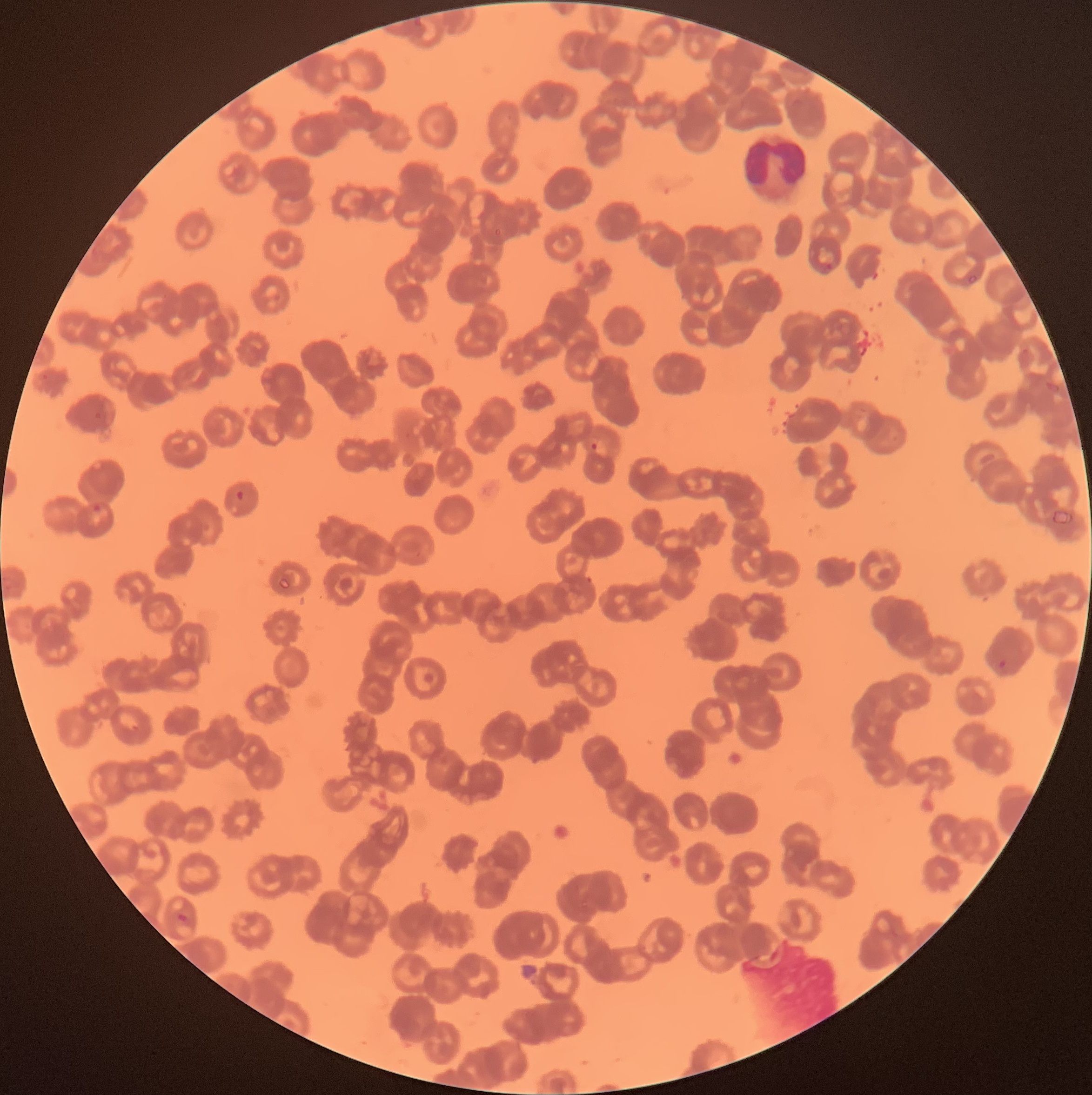

coordinate format = approximate bounding boxes as named x1/y1/x2/y2 corners in pixels
white blood cell locations = (x1=741, y1=134, x2=809, y2=205)
Plasmodium parasite locations = (x1=820, y1=261, x2=834, y2=274), (x1=586, y1=438, x2=599, y2=450), (x1=235, y1=490, x2=246, y2=501), (x1=91, y1=505, x2=106, y2=514), (x1=997, y1=660, x2=1008, y2=669)
preparation = thin blood film
red blood cell morphology = rouleaux formation
image size = 1092×1095 pixels
modality = optical microscopy